Report the malaria status.
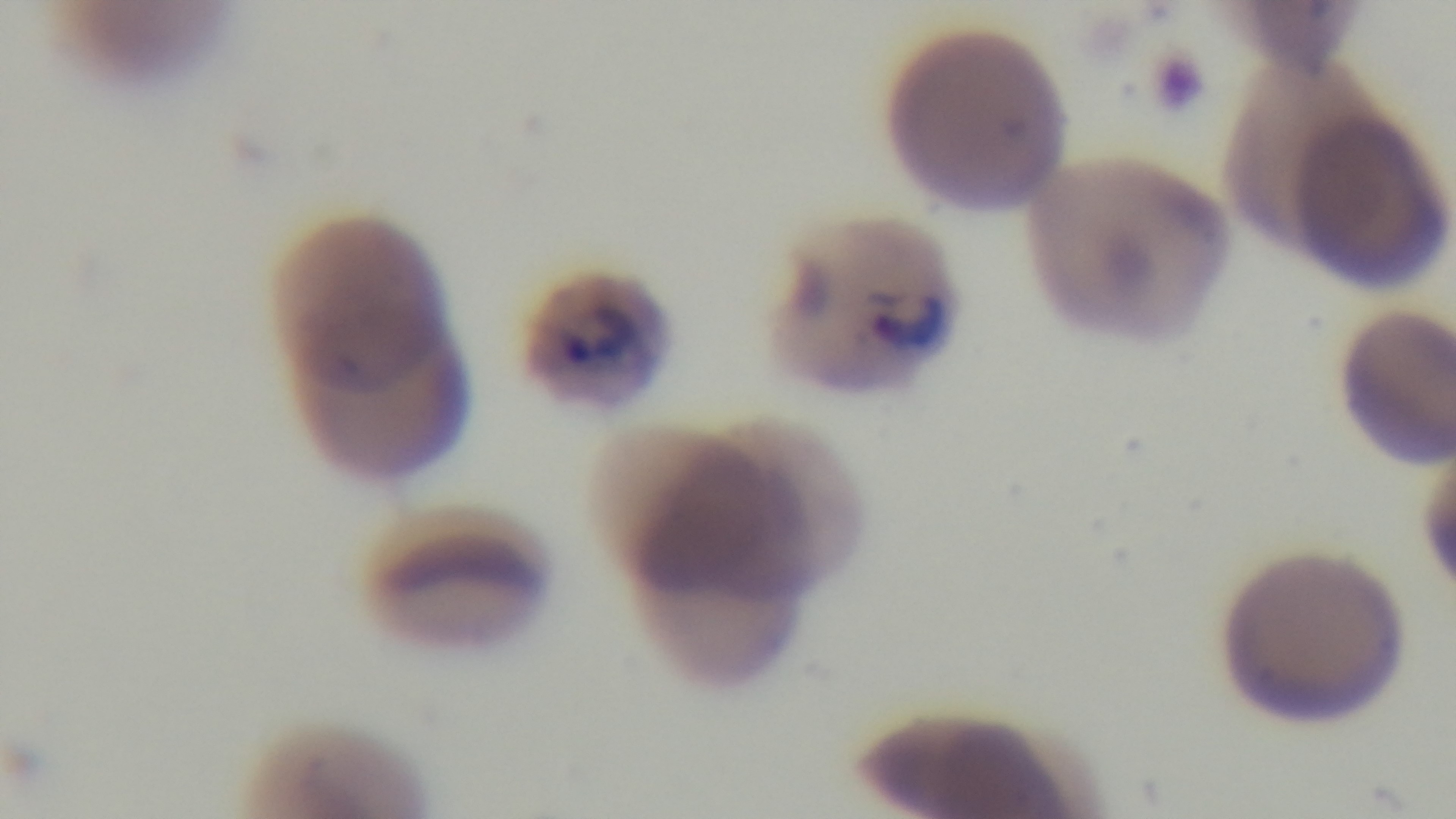

Infected.

Captured with a mounted 4K digital camera. Single field of view. 100x oil-immersion objective. Light microscopy. Giemsa stain. Preparation: thin smear.